Report the malaria status of this cell.
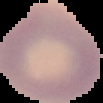
It is uninfected.

Image is 103×103 pixels. The area outside the segmented cell region is set to black. From a thin blood smear.